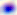

magnification = 400x
modality = micrograph
identification = Toxoplasma gondii